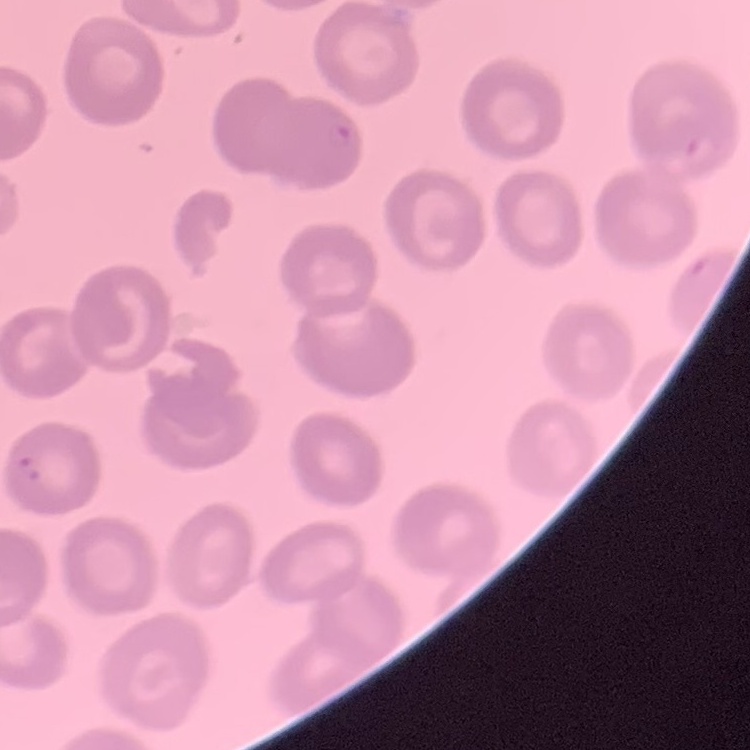

Summary:
  - Erythrocyte morphology: no rouleaux formation
  - Image type: one tile cut from a larger photomicrograph
  - Stain: Field's or Giemsa
  - Preparation: thin peripheral smear